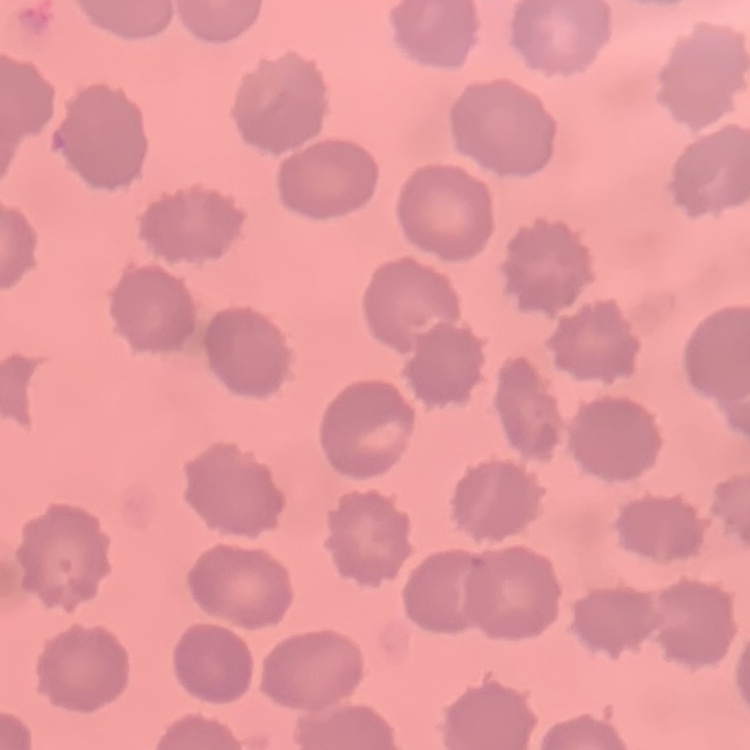

Summary:
  - Erythrocyte morphology: no rouleaux formation
  - Image type: one tile cut from a larger photomicrograph
  - Preparation: thin blood smear
  - Stain: Field's or Giemsa